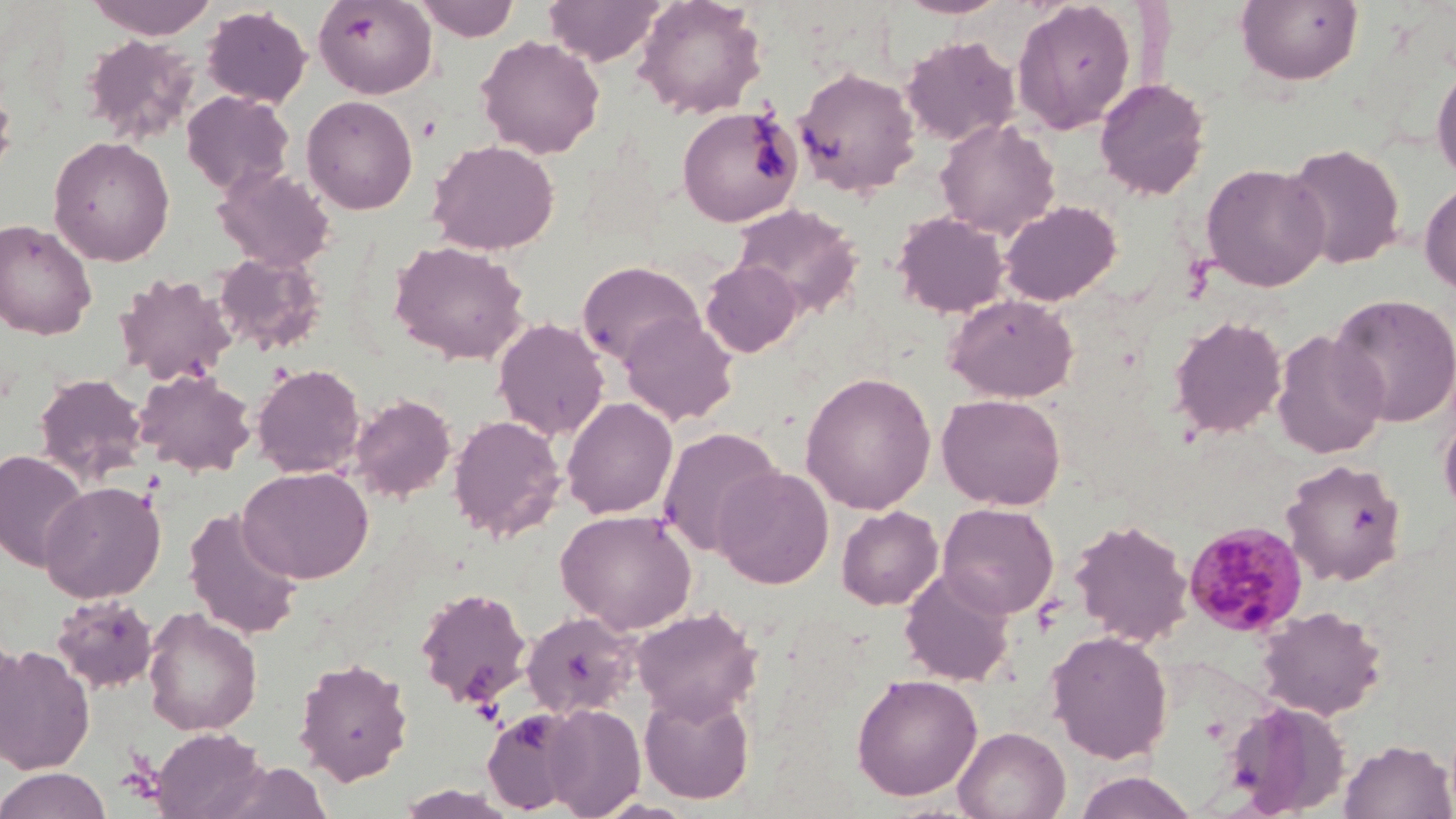

Approximate bounding boxes as (x1, y1, x2, y2) in pixels. Plasmodium malariae-infected red blood cell locations: (1182, 520, 1310, 638). Uninfected red blood cell locations: (84, 0, 219, 40), (312, 0, 438, 99), (414, 0, 519, 42), (542, 0, 665, 66), (634, 0, 768, 119), (893, 0, 1014, 19), (1011, 1, 1137, 135), (1236, 1, 1363, 86), (201, 5, 312, 108), (80, 34, 200, 145), (476, 35, 605, 159), (900, 35, 1020, 147), (1431, 59, 1456, 185), (793, 66, 920, 197), (0, 72, 17, 188), (1094, 77, 1211, 200), (181, 90, 294, 196), (301, 94, 419, 215), (676, 106, 802, 227), (935, 117, 1060, 239), (48, 135, 175, 266), (426, 139, 560, 255), (1283, 143, 1407, 270), (1201, 162, 1330, 292), (212, 164, 337, 272), (1419, 181, 1456, 294), (999, 200, 1122, 306), (731, 203, 863, 319), (892, 211, 1010, 318), (0, 218, 97, 340), (389, 238, 530, 365), (212, 250, 327, 356), (701, 259, 803, 357), (577, 260, 704, 368), (115, 272, 236, 386), (945, 293, 1079, 403), (1328, 293, 1456, 427), (619, 311, 739, 426), (1168, 315, 1288, 438), (492, 317, 610, 441), (1270, 329, 1388, 459), (251, 362, 366, 478), (134, 367, 257, 477), (800, 371, 937, 514), (33, 372, 148, 483), (349, 393, 458, 502), (937, 393, 1066, 510), (561, 396, 678, 519), (1439, 413, 1456, 522), (448, 414, 567, 541), (658, 426, 783, 557), (0, 449, 90, 571), (1280, 458, 1407, 586), (239, 466, 373, 583), (713, 466, 834, 589), (40, 479, 166, 603), (938, 502, 1059, 619), (836, 505, 943, 610), (183, 506, 304, 639), (555, 508, 698, 634), (1068, 518, 1194, 647), (899, 567, 1016, 687), (416, 586, 533, 708), (50, 593, 159, 695), (1256, 605, 1387, 721), (142, 606, 263, 736), (631, 606, 761, 724), (520, 611, 640, 719), (1045, 630, 1174, 764), (0, 632, 28, 761), (0, 643, 95, 775), (293, 657, 413, 785), (851, 673, 983, 801), (639, 687, 755, 804), (1224, 700, 1350, 817), (542, 703, 646, 818), (482, 708, 582, 813), (954, 726, 1071, 819), (150, 728, 268, 819), (1340, 739, 1455, 819), (213, 761, 332, 819), (0, 768, 111, 819), (1072, 771, 1199, 819), (395, 785, 519, 819). Slide-level diagnosis: Plasmodium malariae. Optical microscopy. Image is 1456×819 pixels. 1000x magnification. Thin blood smear. May-Grünwald-Giemsa-stained preparation. One field of a larger specimen.